Assess for Plasmodium parasites.
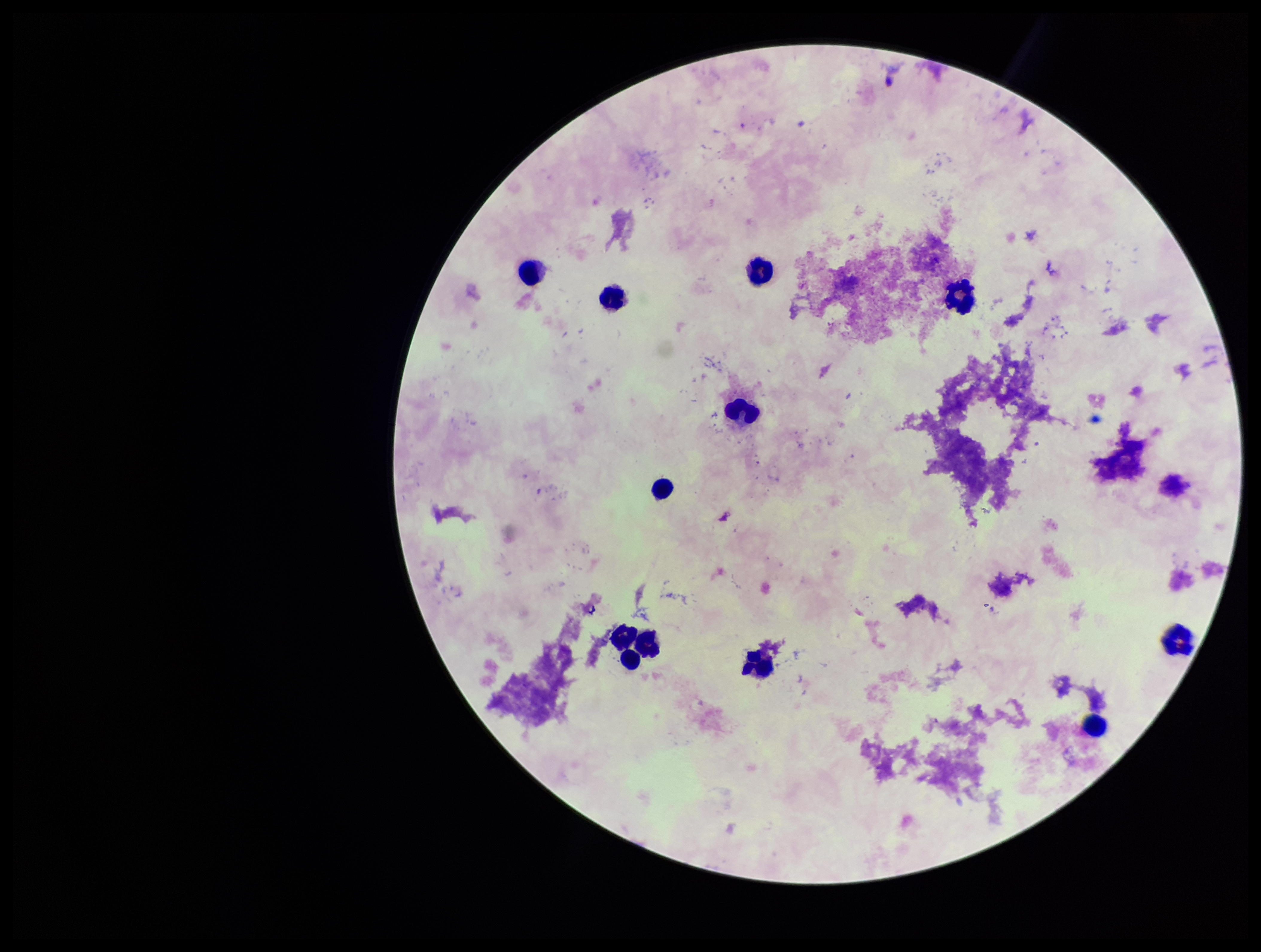

None seen.

Summary:
  - Image size: 1261×952 pixels
  - Preparation: thick
  - Field of view: one from this slide
  - Patient malaria status: negative
  - Leukocyte count: 12
  - Parasite count: 0
  - Capture: smartphone photograph through the microscope eyepiece
  - Stain: Giemsa